Classify this cell by malaria status.
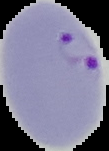
It is parasitized.

preparation = thin blood film
image size = 109×151 pixels
image type = cell region segmented out of the field of view; surrounding area masked to black